Classify this cell by malaria status.
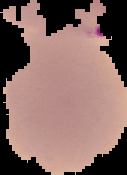

It is uninfected.

Summary:
  - Image size: 127×175 pixels
  - Image type: segmented cell region with the area outside set to black
  - Preparation: thin blood film